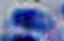
Photomicrograph. 1000x magnification. Toxoplasma gondii is shown.